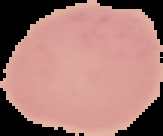

image_size: 163×136 pixels
malaria_status: uninfected
image_type: cell region segmented out of the field of view; surrounding area masked to black
preparation: thin blood film